Report the malaria status of this cell.
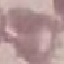
Uninfected.

Summary:
  - Preparation: thin blood film
  - Stain: Giemsa
  - Image type: automatically extracted cell patch, resized to 64 × 64 pixels
  - Capture: smartphone through the microscope eyepiece